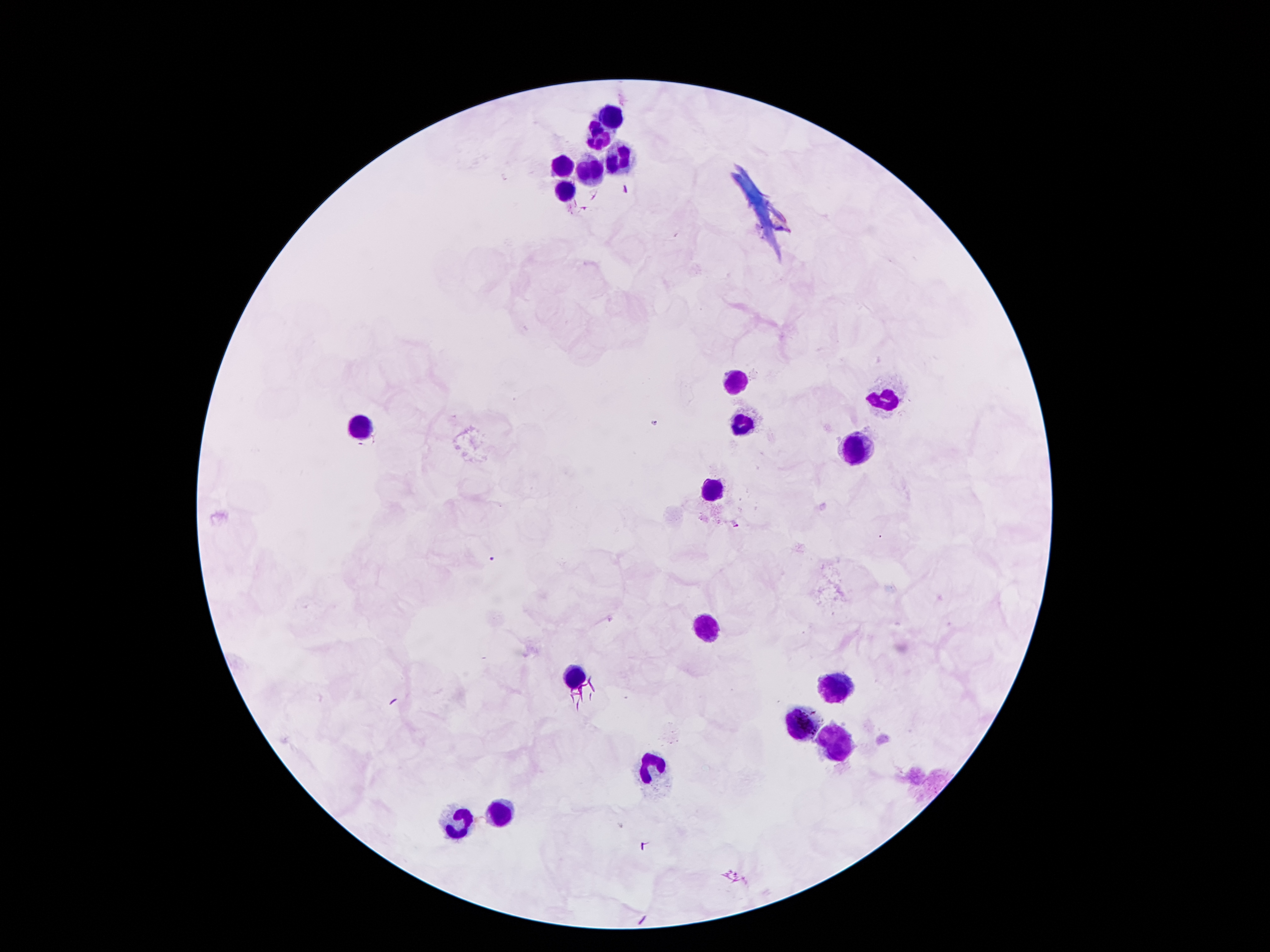

Approximate centers as {x, y} in pixels.
Summary:
  - Leukocyte locations: {613, 115}, {598, 137}, {618, 159}, {564, 167}, {591, 169}, {566, 188}, {735, 382}, {885, 399}, {740, 424}, {361, 426}, {858, 444}, {713, 490}, {703, 631}, {572, 676}, {838, 686}, {804, 727}, {833, 742}, {653, 767}, {502, 810}, {456, 822}
  - Plasmodium parasite locations: {625, 189}, {736, 524}, {492, 559}
  - Capture: smartphone through the microscope eyepiece
  - Patient malaria status: infected with Plasmodium falciparum
  - Preparation: thick blood smear
  - Magnification: 100x
  - Image size: 1270×952 pixels
  - Field of view: one from this slide
  - Stain: Giemsa